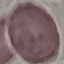 Result: no malaria parasites detected. Cell patch, automatically extracted from a larger field of view and resized to 64 × 64 pixels. Thin smear of blood. Acquired by smartphone through the microscope eyepiece. Giemsa-stained preparation.